Describe the morphology of the red blood cells.
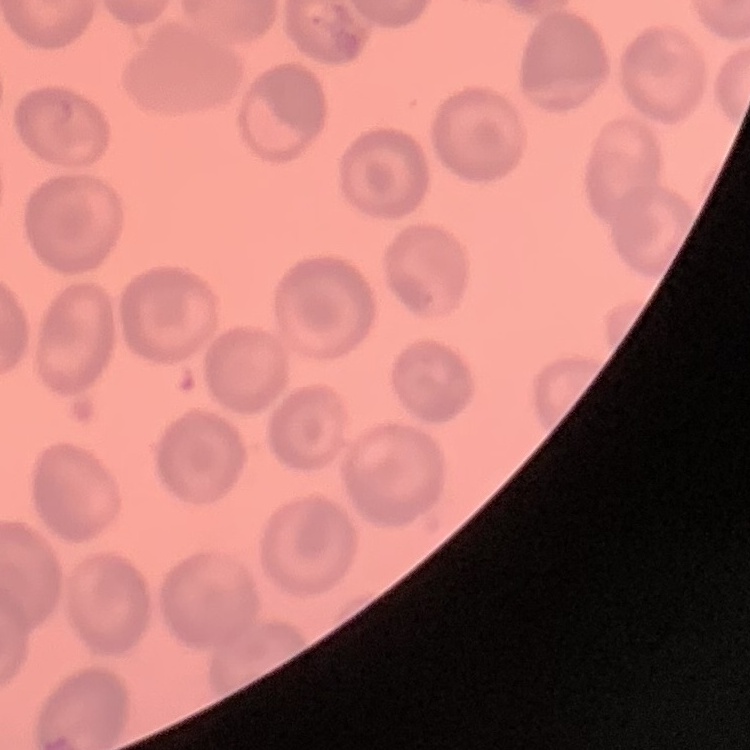
They show no rouleaux formation.

One tile cut from a larger photomicrograph. Thin blood film. Stained with either Field's or Giemsa.